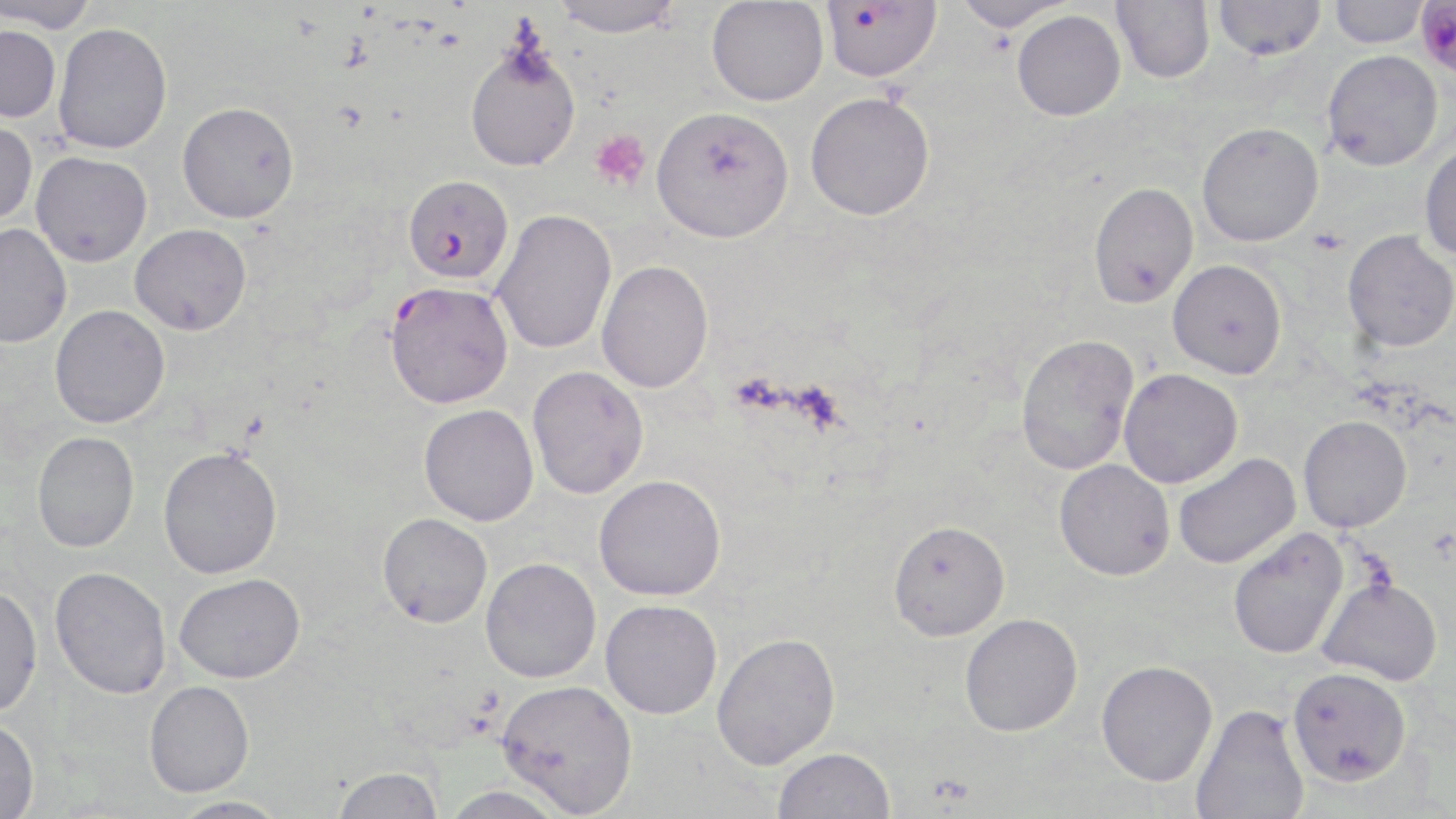

Approximate bounding boxes as [x1, y1, x2, y2] in pixels. Platelet locations: [588, 129, 652, 191], [1308, 227, 1348, 256]. Uninfected red blood cell locations: [549, 0, 685, 37], [951, 0, 1075, 31], [1111, 0, 1215, 83], [2, 1, 99, 33], [706, 1, 828, 106], [1213, 1, 1327, 61], [1328, 1, 1431, 48], [1012, 10, 1126, 121], [54, 22, 172, 154], [0, 25, 61, 122], [465, 43, 582, 172], [1322, 49, 1443, 171], [805, 91, 935, 221], [177, 101, 300, 222], [650, 106, 794, 243], [0, 118, 38, 226], [1197, 121, 1324, 246], [1419, 142, 1456, 262], [31, 151, 152, 266], [1088, 182, 1198, 309], [491, 209, 617, 354], [130, 223, 251, 336], [0, 224, 72, 348], [1342, 229, 1456, 352], [1167, 259, 1287, 379], [596, 260, 714, 393], [50, 304, 169, 428], [1015, 333, 1140, 475], [527, 366, 649, 499], [1119, 368, 1242, 488], [419, 404, 539, 526], [1298, 415, 1411, 533], [32, 431, 139, 553], [158, 446, 282, 578], [1173, 453, 1301, 569], [1054, 459, 1175, 581], [594, 474, 726, 601], [377, 513, 493, 628], [887, 519, 1010, 641], [1227, 527, 1349, 659], [480, 557, 602, 683], [49, 567, 172, 699], [175, 572, 305, 683], [1317, 577, 1444, 686], [0, 584, 43, 718], [600, 599, 722, 720], [959, 613, 1083, 737], [711, 632, 841, 769], [1096, 659, 1218, 786], [1287, 666, 1411, 787], [496, 679, 639, 816], [144, 680, 254, 797], [1190, 704, 1309, 819], [0, 719, 40, 818], [772, 747, 896, 819], [331, 766, 444, 819], [439, 785, 572, 819], [167, 796, 292, 819]. Plasmodium falciparum-infected red blood cell locations: [1417, 0, 1456, 74], [821, 1, 942, 82], [403, 174, 514, 285], [384, 281, 513, 408]. Slide-level diagnosis: Plasmodium falciparum. Image is 1456×819 pixels. Optical microscopy. May-Grünwald-Giemsa-stained preparation. Captured at 1000x magnification. Thin blood smear. One field of a larger specimen.